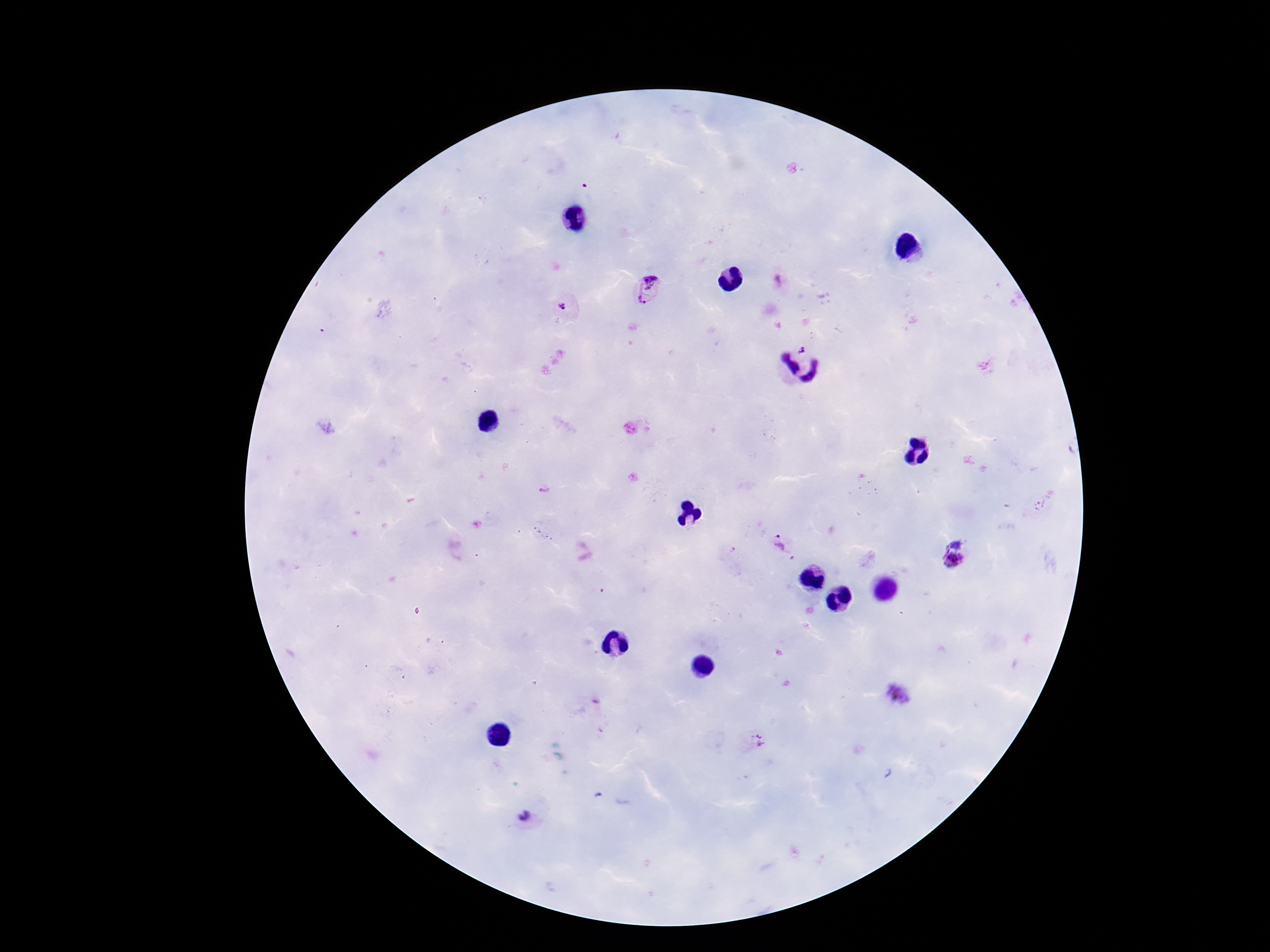

field of view = single
preparation = thick blood film
Plasmodium parasite locations = approximate centers as [x, y] in pixels: [650, 278], [638, 303], [563, 306], [543, 489], [781, 544], [951, 560], [897, 694], [755, 742], [525, 819]
patient malaria status = infected
magnification = 100x
stain = Giemsa
image size = 1270×952 pixels
capture = smartphone camera through the microscope eyepiece